Point out Plasmodium parasites and leukocytes.
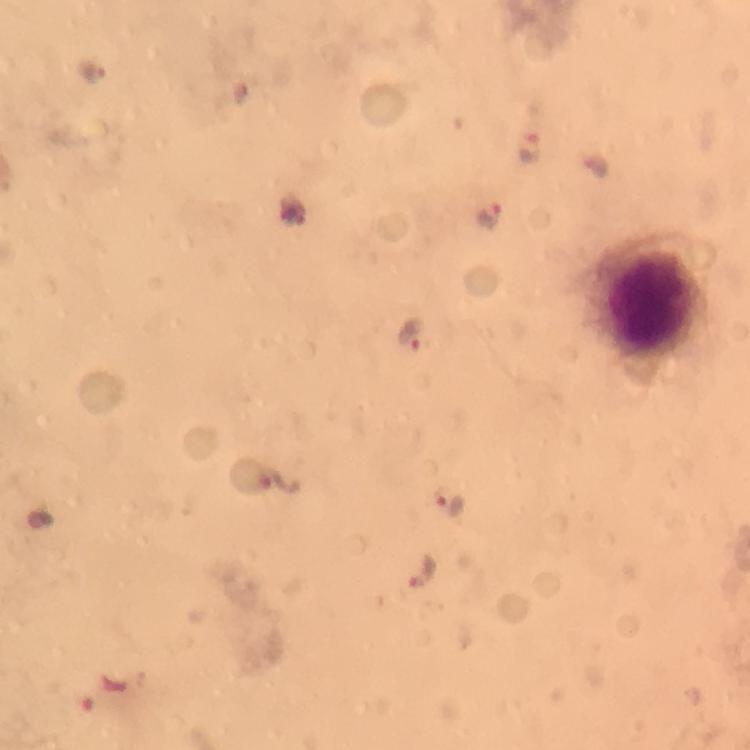

Approximate centers as [x, y] in pixels.
Plasmodium parasites: [92, 71], [528, 146], [491, 215], [410, 333], [281, 480], [448, 505], [424, 573].
Leukocytes: [655, 293].

100x magnification. From a malaria diagnostic workup. Thick blood film. Cropped region of a single field of view. Smartphone photograph taken through a microscope. Giemsa stain. Immersion oil was used. Image is 750×750 pixels.